Assess the morphology of the red blood cells.
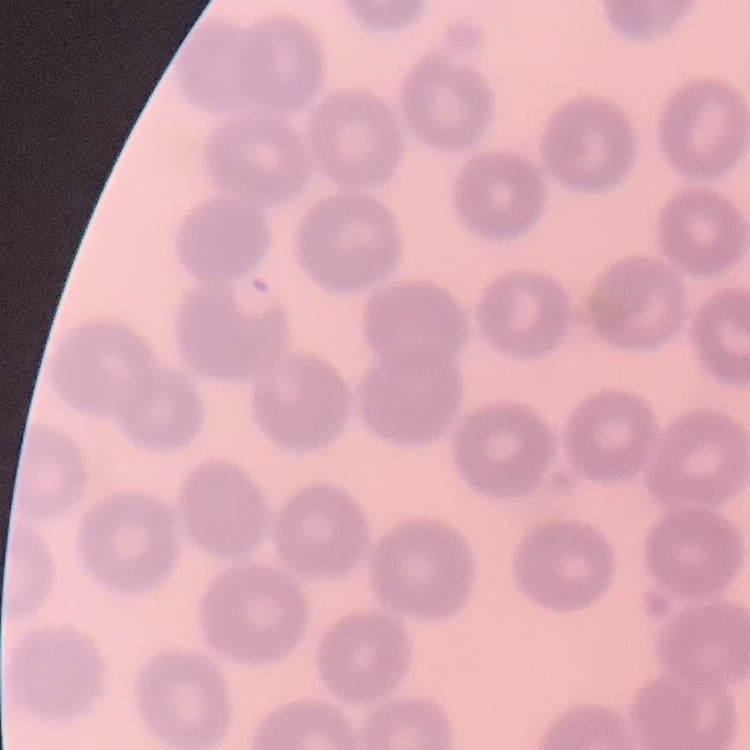

They show no rouleaux formation.

Summary:
  - Preparation: thin blood smear
  - Image type: one tile cut from a larger photomicrograph
  - Stain: Field's or Giemsa